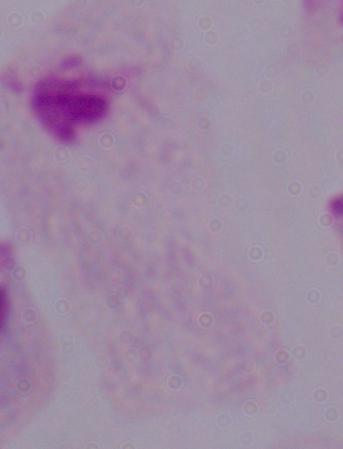

Summary:
  - Magnification: 1000x
  - Identification: trichomonad
  - Modality: micrograph